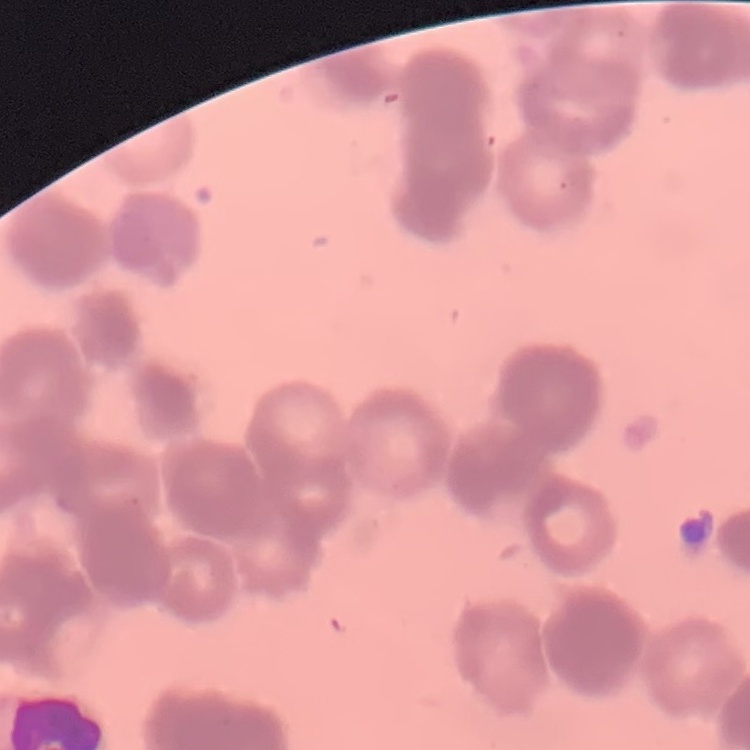

red_blood_cell_morphology: rouleaux formation
image_type: square crop of a larger photomicrograph
stain: Field's or Giemsa
preparation: thin peripheral smear